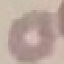
malaria status = uninfected
image type = cell patch, automatically extracted from a larger field of view and resized to 64 × 64 pixels
capture = smartphone camera at the microscope eyepiece
stain = Giemsa
preparation = thin blood smear